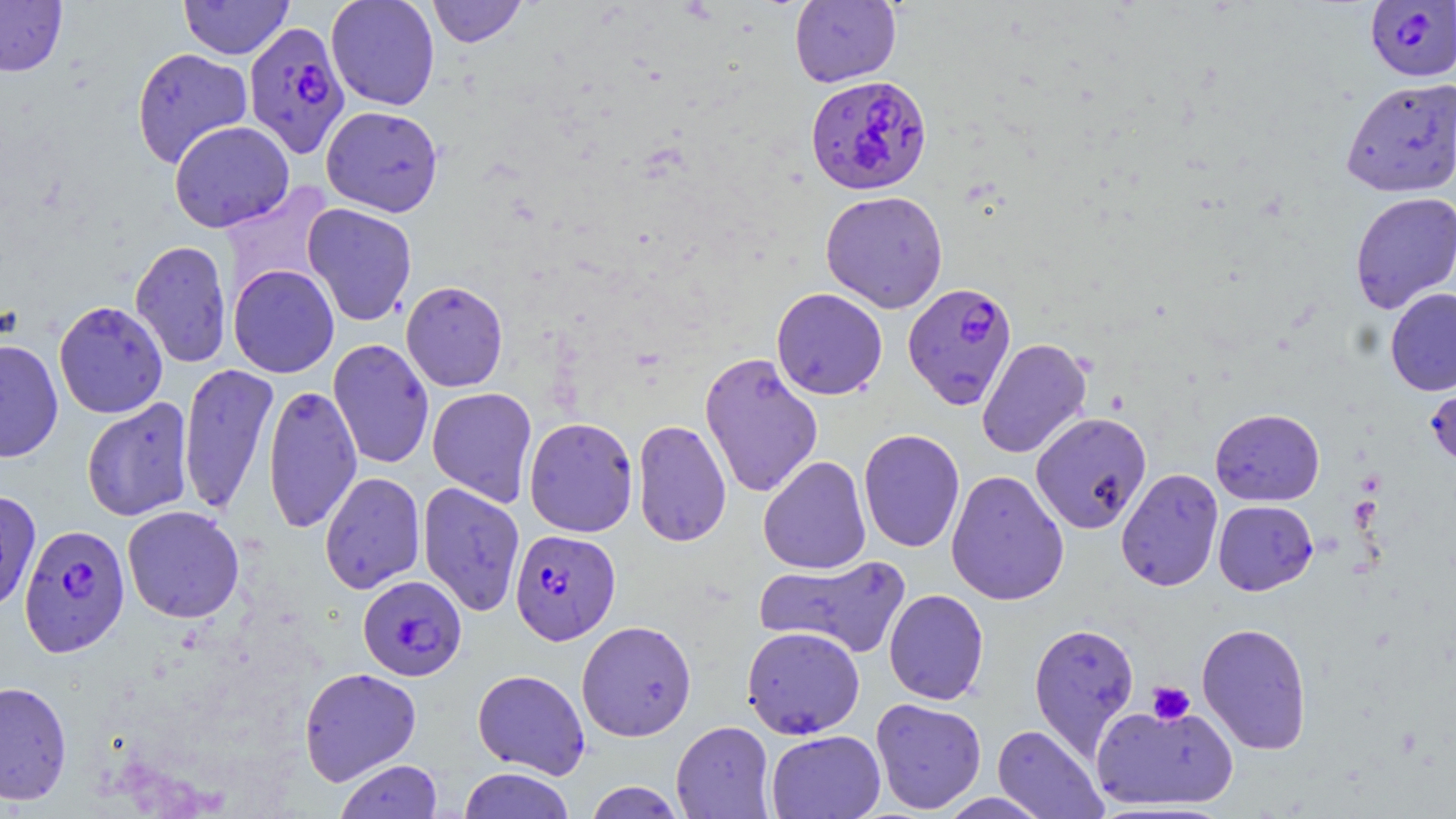
Approximate bounding boxes as [x1, y1, x2, y2] in pixels. Plasmodium falciparum-infected red blood cell locations: [1364, 1, 1456, 82], [243, 20, 350, 158], [805, 74, 932, 195], [902, 282, 1017, 409], [19, 523, 130, 656], [510, 529, 620, 645], [357, 575, 467, 681]. Uninfected red blood cell locations: [0, 0, 68, 76], [179, 0, 294, 59], [326, 0, 441, 111], [427, 0, 527, 48], [789, 1, 901, 87], [131, 47, 253, 169], [1340, 77, 1456, 198], [321, 105, 443, 217], [169, 120, 294, 232], [220, 182, 335, 299], [820, 190, 948, 313], [1349, 191, 1456, 314], [302, 203, 418, 326], [130, 240, 233, 368], [228, 264, 339, 378], [400, 280, 508, 393], [772, 287, 888, 400], [1385, 288, 1456, 396], [53, 300, 168, 419], [0, 338, 63, 463], [976, 338, 1092, 459], [328, 339, 434, 469], [699, 351, 823, 499], [179, 363, 279, 516], [1425, 367, 1456, 473], [263, 383, 362, 535], [427, 387, 538, 507], [81, 398, 194, 522], [1210, 408, 1325, 506], [1030, 411, 1152, 534], [523, 416, 639, 537], [632, 419, 732, 548], [858, 429, 966, 553], [758, 455, 872, 575], [1116, 468, 1223, 592], [945, 469, 1070, 606], [319, 471, 426, 594], [418, 482, 525, 617], [0, 488, 41, 612], [1213, 500, 1318, 595], [122, 505, 245, 623], [754, 555, 912, 660], [884, 589, 989, 705], [576, 620, 697, 741], [1196, 621, 1312, 754], [1028, 622, 1140, 758], [741, 625, 865, 739], [298, 667, 422, 786], [472, 669, 591, 778], [0, 680, 73, 805], [870, 697, 986, 814], [1089, 701, 1239, 810], [671, 721, 775, 818], [992, 724, 1107, 818], [766, 730, 885, 819], [335, 759, 443, 818], [458, 767, 576, 819], [584, 781, 686, 818], [938, 792, 1054, 819]. Platelet locations: [1147, 681, 1195, 725]. Slide-level diagnosis: Plasmodium falciparum. May-Grünwald-Giemsa stain. Thin blood smear. 1000x magnification. Image is 1456×819 pixels. Single field of view. Light microscopy.